Assess the morphology of the red blood cells.
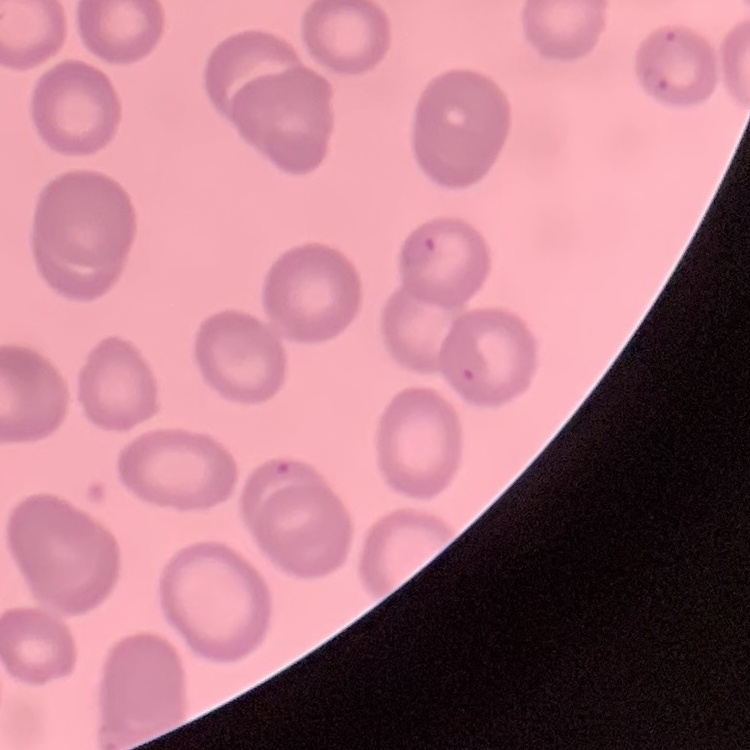

They show no rouleaux formation.

Summary:
  - Image type: one tile cut from a larger photomicrograph
  - Stain: Field's or Giemsa
  - Preparation: thin blood film